Give the position of every Plasmodium parasite visible.
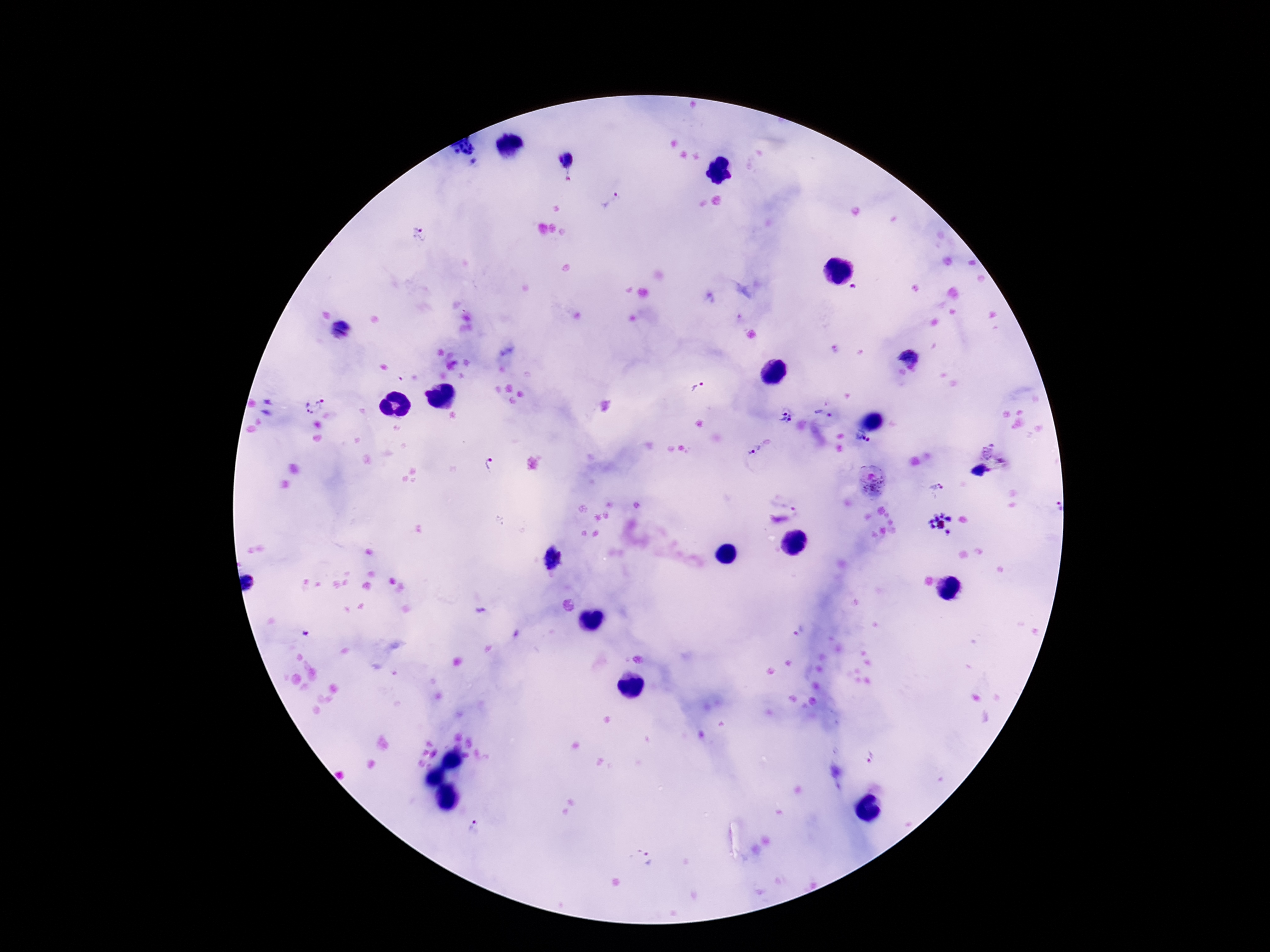
Approximate centers as {x, y} in pixels.
Plasmodium parasites: {468, 152}, {568, 156}, {609, 201}, {419, 235}, {854, 287}, {340, 331}, {909, 354}, {699, 385}, {311, 402}, {818, 411}, {786, 417}, {862, 439}, {754, 448}, {996, 453}, {491, 465}, {872, 484}, {937, 488}, {1056, 507}, {940, 524}, {554, 558}, {251, 581}, {872, 757}, {472, 826}, {647, 859}.

Smartphone photograph taken through the microscope eyepiece. Image is 1270×952 pixels. Giemsa stain. 100x magnification. Patient malaria status: positive. One field from this slide. Thick blood film.